State the blood parasite species.
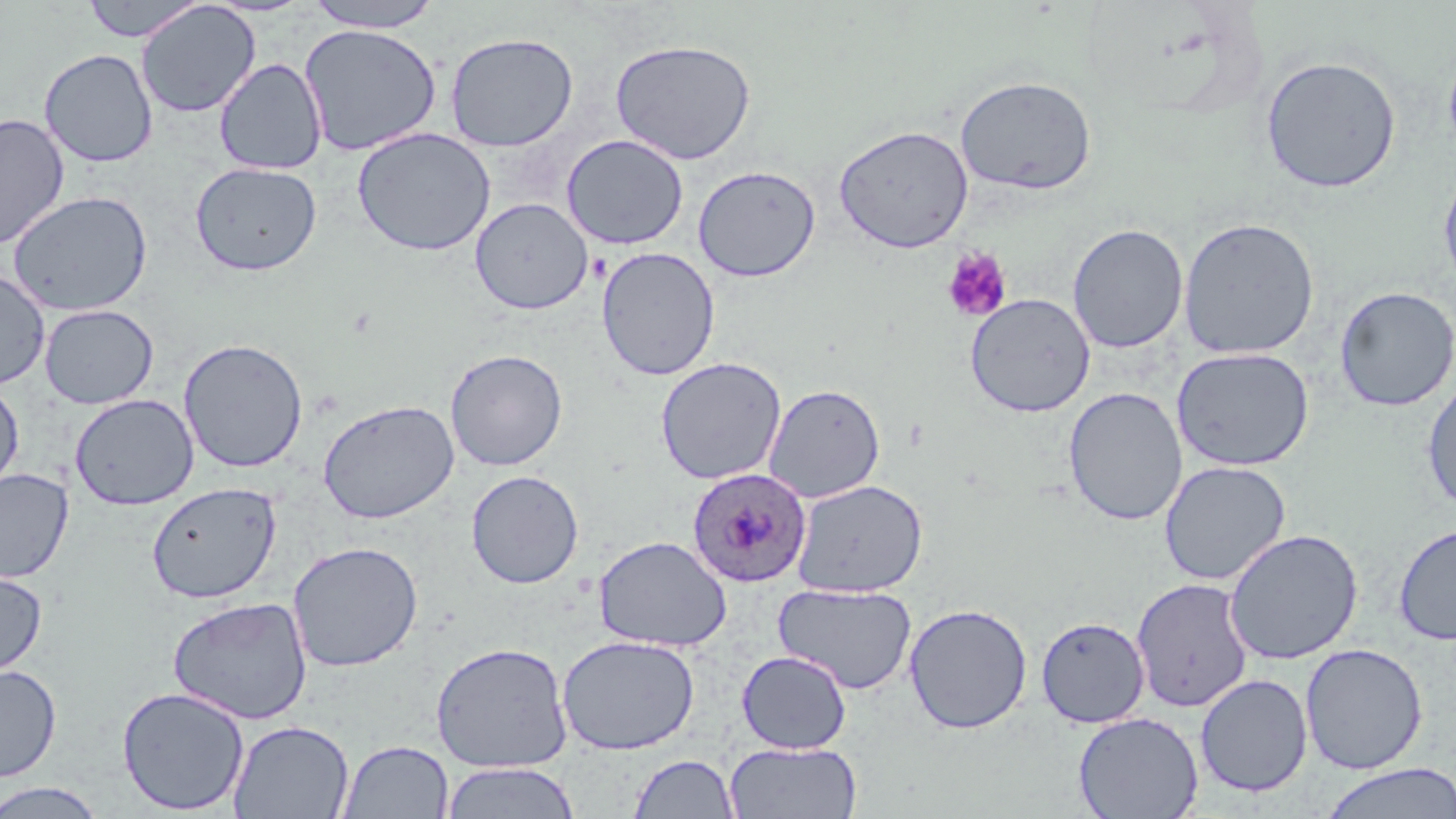
Plasmodium ovale.

{
  "stain": "May-Grünwald-Giemsa",
  "platelet_locations": "approximate bounding boxes as (x1, y1, x2, y2) in pixels: (942, 249, 1012, 322)",
  "uninfected_red_blood_cell_locations": "approximate bounding boxes as (x1, y1, x2, y2) in pixels: (79, 0, 206, 42), (305, 0, 441, 32), (136, 1, 261, 118), (299, 23, 442, 156), (445, 32, 579, 152), (610, 39, 757, 164), (1442, 40, 1456, 169), (39, 49, 158, 168), (1260, 55, 1401, 193), (214, 58, 327, 175), (955, 75, 1097, 195), (0, 113, 70, 250), (833, 124, 974, 253), (352, 127, 496, 256), (561, 134, 688, 249), (190, 161, 322, 276), (693, 165, 820, 282), (1437, 165, 1456, 295), (6, 190, 153, 317), (470, 197, 593, 314), (1178, 217, 1320, 360), (1067, 223, 1188, 354), (596, 247, 720, 381), (0, 268, 51, 389), (1333, 286, 1456, 412), (965, 293, 1096, 417), (39, 304, 159, 409), (178, 338, 308, 474), (1171, 347, 1314, 471), (445, 349, 568, 471), (655, 357, 786, 485), (1421, 375, 1456, 515), (0, 379, 24, 495), (764, 383, 886, 503), (1063, 387, 1187, 526), (69, 393, 199, 510), (318, 399, 459, 524), (1158, 460, 1292, 586), (0, 468, 74, 583), (466, 470, 584, 588), (792, 479, 928, 597), (146, 482, 282, 603), (1393, 522, 1456, 646), (1224, 528, 1363, 665), (594, 535, 732, 651), (287, 541, 423, 672), (0, 569, 48, 679), (1131, 577, 1254, 712), (773, 583, 917, 694), (168, 596, 313, 725), (903, 603, 1032, 733), (1036, 616, 1150, 728), (556, 634, 700, 755), (430, 641, 573, 772), (1300, 642, 1428, 774), (736, 650, 852, 754), (0, 664, 61, 782), (1195, 673, 1313, 797), (116, 687, 250, 815), (1073, 711, 1203, 819), (228, 720, 354, 819), (338, 740, 453, 818), (725, 741, 862, 819), (627, 754, 740, 818), (441, 761, 579, 819), (1318, 762, 1456, 819), (0, 782, 107, 818)",
  "modality": "optical microscopy",
  "image_size": "1456×819 pixels",
  "magnification": "1000x",
  "field_of_view": "one of a larger specimen",
  "preparation": "thin blood film",
  "plasmodium_ovale_infected_red_blood_cell_locations": "approximate bounding boxes as (x1, y1, x2, y2) in pixels: (686, 467, 812, 587)"
}